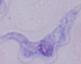

{
  "modality": "micrograph",
  "magnification": "1000x",
  "identification": "trypanosome"
}